Find each white blood cell.
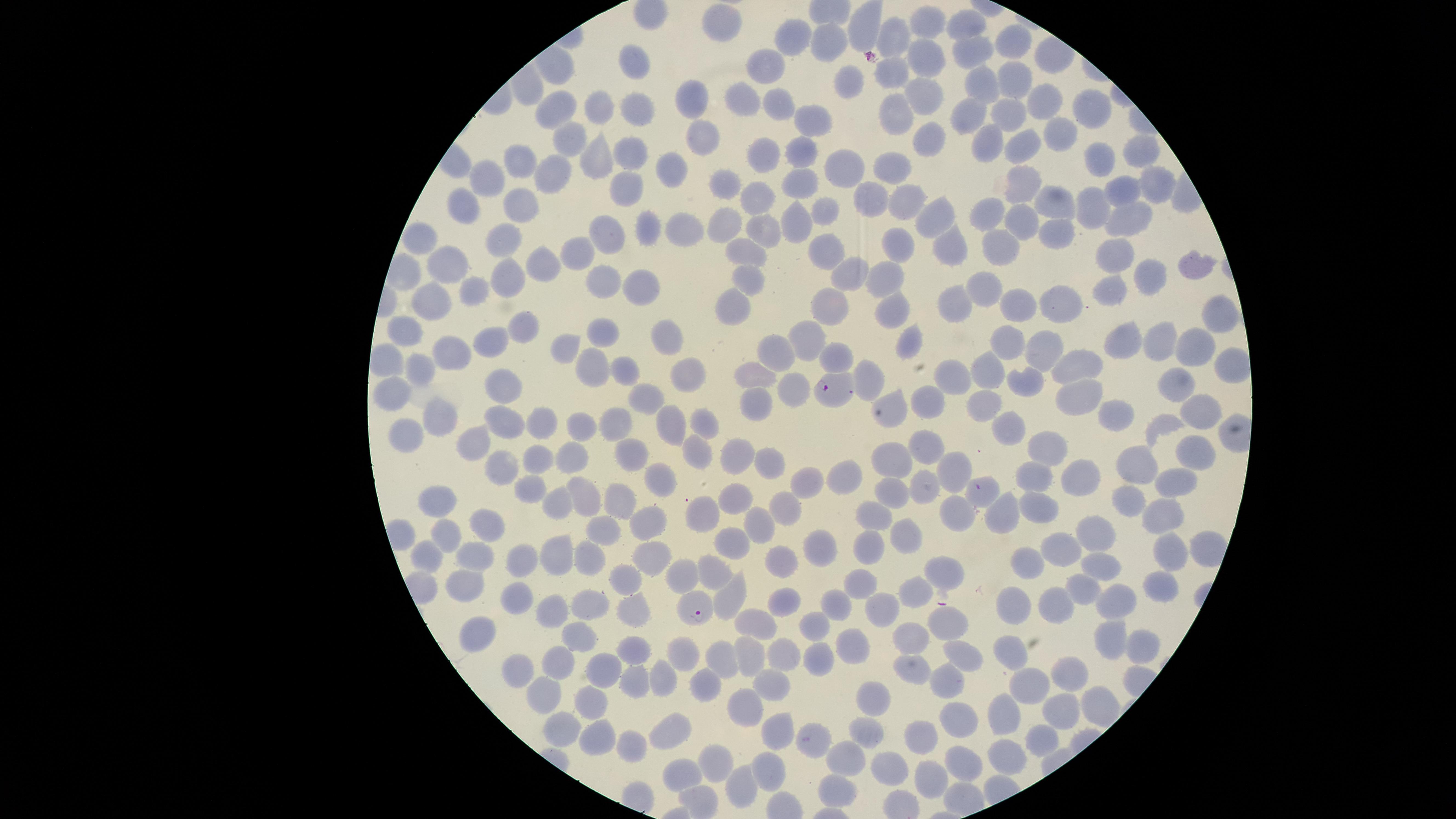
No white blood cells identified.

Approximate marker points as [x, y] in pixels. Parasitized red blood cells: [833, 388], [697, 609]. Uninfected red blood cells: [967, 24], [927, 25], [716, 26], [895, 37], [793, 40], [1010, 45], [826, 48], [971, 51], [926, 57], [769, 64], [636, 69], [895, 70], [1008, 75], [850, 79], [981, 82], [923, 89], [741, 99], [1036, 99], [695, 103], [779, 103], [971, 110], [634, 112], [601, 113], [1081, 113], [564, 115], [895, 115], [1009, 122], [811, 123], [701, 132], [1050, 132], [931, 133], [568, 140], [990, 140], [1013, 144], [799, 146], [1140, 147], [1099, 150], [766, 153], [632, 157], [592, 159], [520, 161], [892, 161], [843, 164], [675, 166], [556, 172], [801, 175], [486, 179], [1154, 179], [727, 182], [1024, 183], [624, 189], [1126, 189], [761, 193], [873, 196], [519, 197], [1058, 198], [461, 200], [905, 203], [830, 209], [1099, 209], [993, 212], [929, 215], [1133, 215], [798, 219], [1021, 219], [726, 220], [760, 224], [684, 225], [652, 226], [610, 230], [1056, 231], [505, 234], [416, 237], [946, 241], [895, 244], [999, 244], [750, 246], [1116, 249], [576, 252], [824, 254], [543, 263], [456, 266], [1187, 268], [843, 271], [1148, 271], [885, 276], [598, 280], [750, 281], [506, 282], [642, 282], [474, 286], [1118, 287], [988, 290], [1018, 302], [958, 303], [428, 305], [1059, 305], [834, 306], [732, 308], [889, 308], [1213, 311], [528, 321], [607, 327], [405, 329], [673, 330], [814, 338], [1117, 340], [907, 341], [490, 342], [1011, 342], [1147, 342], [565, 349], [1044, 349], [1186, 349], [454, 352], [1080, 355], [841, 356], [385, 358], [778, 359], [421, 367], [595, 368], [685, 369], [981, 369], [627, 370], [1227, 371], [754, 373], [869, 376], [956, 376], [1026, 377], [508, 388], [791, 388], [1177, 388], [392, 392], [1079, 397], [650, 398], [928, 399], [897, 401], [986, 402], [752, 403], [1204, 410], [1114, 415], [442, 418], [618, 419], [503, 422], [669, 423], [703, 423], [1004, 424], [1160, 425], [583, 426], [540, 427], [403, 436], [469, 439], [1043, 442], [630, 449], [920, 449], [697, 451], [742, 451], [1196, 451], [568, 453], [538, 455], [769, 457], [1142, 457], [898, 458], [498, 463], [949, 466], [844, 472], [661, 477], [1040, 477], [1083, 478], [802, 481], [532, 485], [892, 487], [920, 487], [1175, 487], [586, 491], [983, 491], [1138, 495], [736, 496], [565, 498], [440, 501], [620, 501], [787, 506], [1040, 508], [999, 510], [703, 511], [1163, 512], [651, 516], [956, 516], [870, 518], [487, 524], [755, 524], [606, 527], [442, 531], [1101, 531], [732, 539], [905, 540], [1166, 541], [1063, 546], [820, 548], [648, 551], [560, 553], [427, 554], [867, 555], [478, 557], [523, 560], [588, 561], [778, 561], [1029, 562], [1098, 565], [714, 566], [950, 568], [682, 570], [623, 578], [465, 582], [860, 583], [1162, 585], [1083, 586], [918, 587], [729, 589], [1111, 592], [784, 595], [1021, 596], [837, 599], [589, 601], [885, 601], [517, 602], [1058, 603], [552, 607], [629, 608], [755, 622], [951, 622], [812, 627], [473, 632], [1105, 636], [578, 638], [911, 640], [630, 646], [847, 646], [1012, 646], [1138, 646], [748, 648], [782, 653], [682, 654], [967, 654], [562, 657], [818, 660], [608, 661], [912, 664], [718, 667], [517, 669], [1070, 670], [634, 676], [657, 676], [1034, 678], [944, 684], [769, 689], [699, 690], [541, 691], [591, 698], [871, 698], [746, 706], [1004, 707], [1058, 708], [1093, 709], [965, 718], [560, 724], [776, 730], [674, 732], [864, 732], [592, 733], [809, 734], [919, 738], [1042, 740], [630, 742], [714, 756], [1009, 756], [842, 759], [964, 760], [895, 767], [939, 772], [676, 773], [766, 774], [741, 785], [840, 790]. Species: Plasmodium falciparum. Circular visible region. Image is 1456×819 pixels. Presence: malaria parasites detected. Smartphone photograph through the microscope eyepiece. Giemsa-stained preparation. Single field of view. Thin blood film.